State the preparation type.
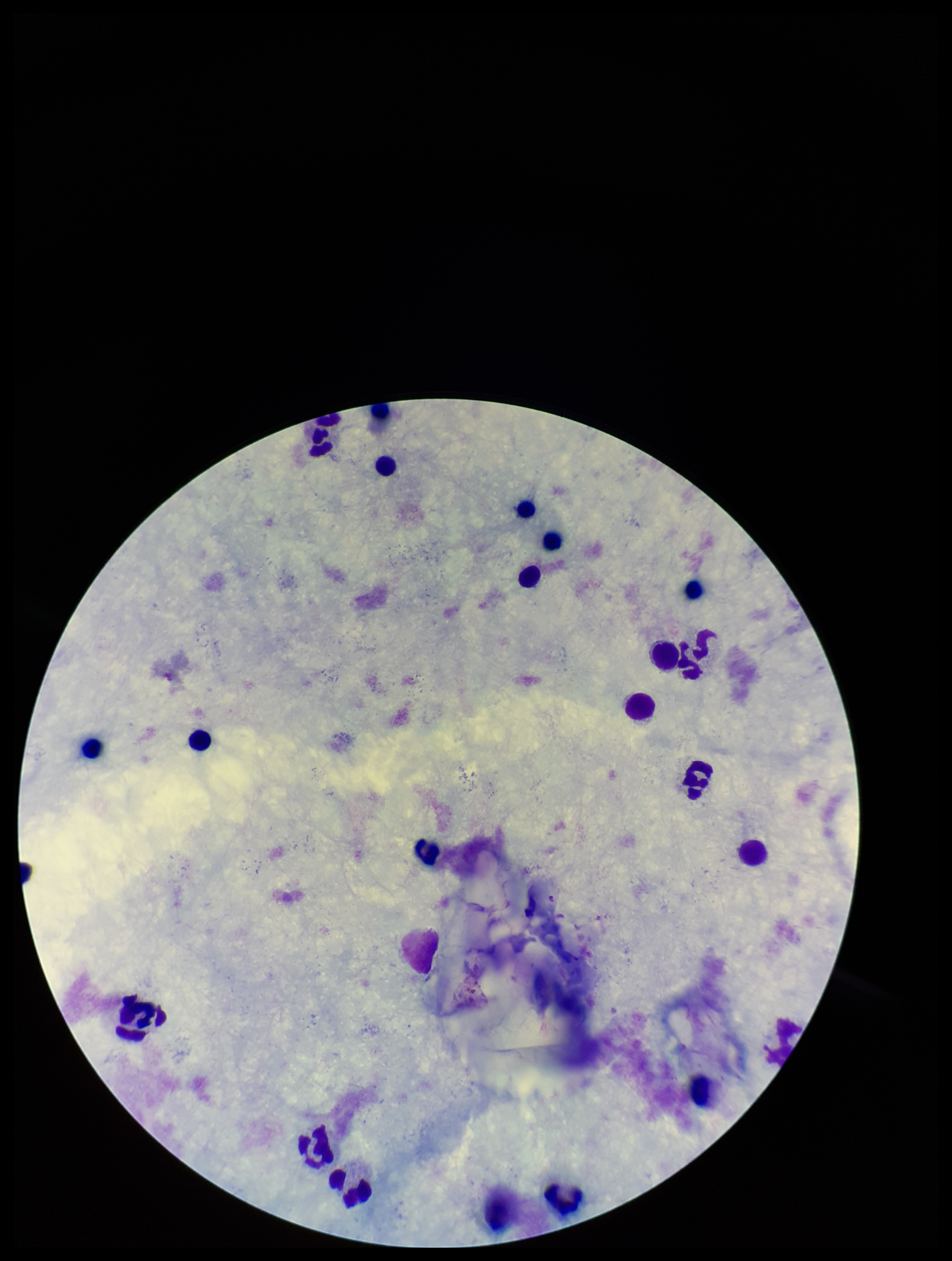

Thick.

Summary:
  - Leukocyte count: 21
  - Stain: Giemsa
  - Plasmodium parasites: none seen
  - Parasite count: 0
  - Image size: 952×1261 pixels
  - Capture: smartphone photograph through the microscope eyepiece
  - Field of view: single
  - Patient malaria status: negative